State the preparation type.
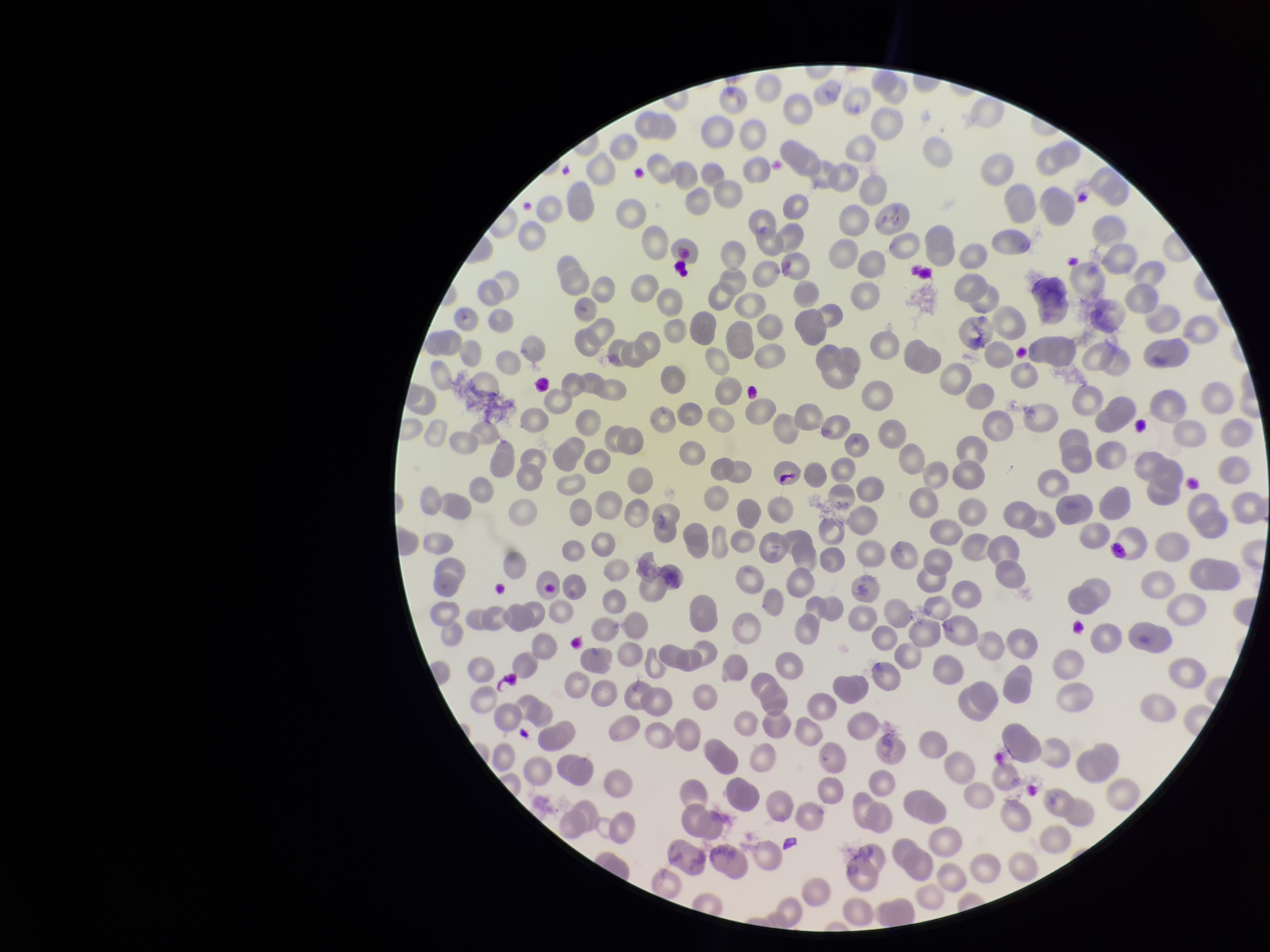
It is a thin blood smear.

{
  "patient_malaria_status": "positive",
  "field_of_view": "one from this slide",
  "species_reported_for_this_patient": "Plasmodium falciparum",
  "parasitized_red_blood_cell_count": 0,
  "red_blood_cell_count": 295,
  "image_size": "1270×952 pixels",
  "stain": "Giemsa",
  "capture": "smartphone photograph through the microscope eyepiece",
  "parasitized_red_blood_cells": "none seen"
}